Give the position of every Plasmodium parasite.
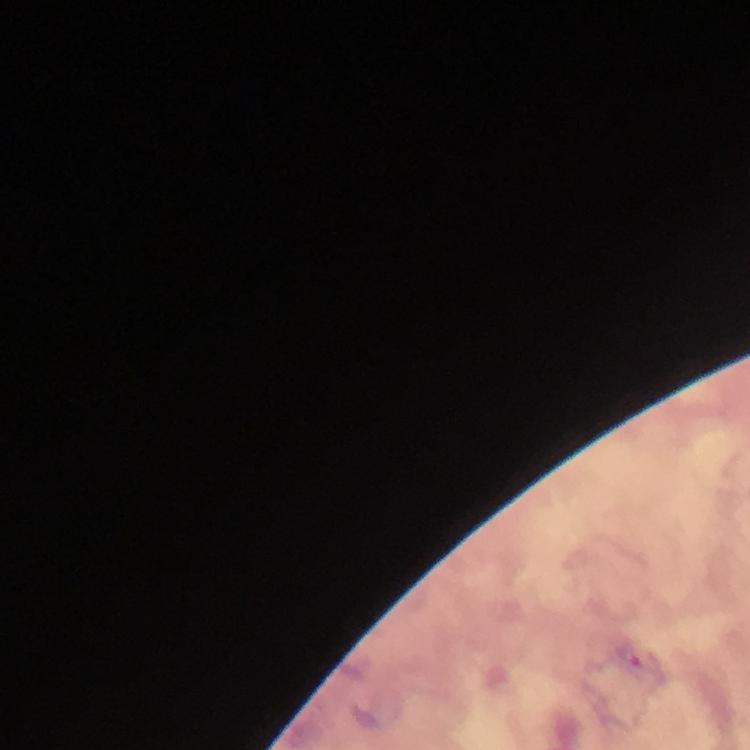

Approximate centers as (x, y) in pixels.
Plasmodium parasites: (631, 655).

Summary:
  - Context: from a diagnostic examination for malaria
  - Immersion oil: applied
  - Image size: 750×750 pixels
  - Magnification: 100x
  - Cropped from: one field of view
  - Preparation: thick smear
  - Stain: Giemsa
  - Capture: smartphone photograph through a microscope